Name the cell type shown.
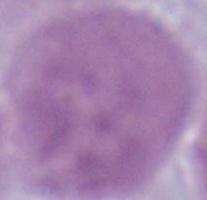
This is an erythrocyte.

1000x magnification. Photomicrograph.